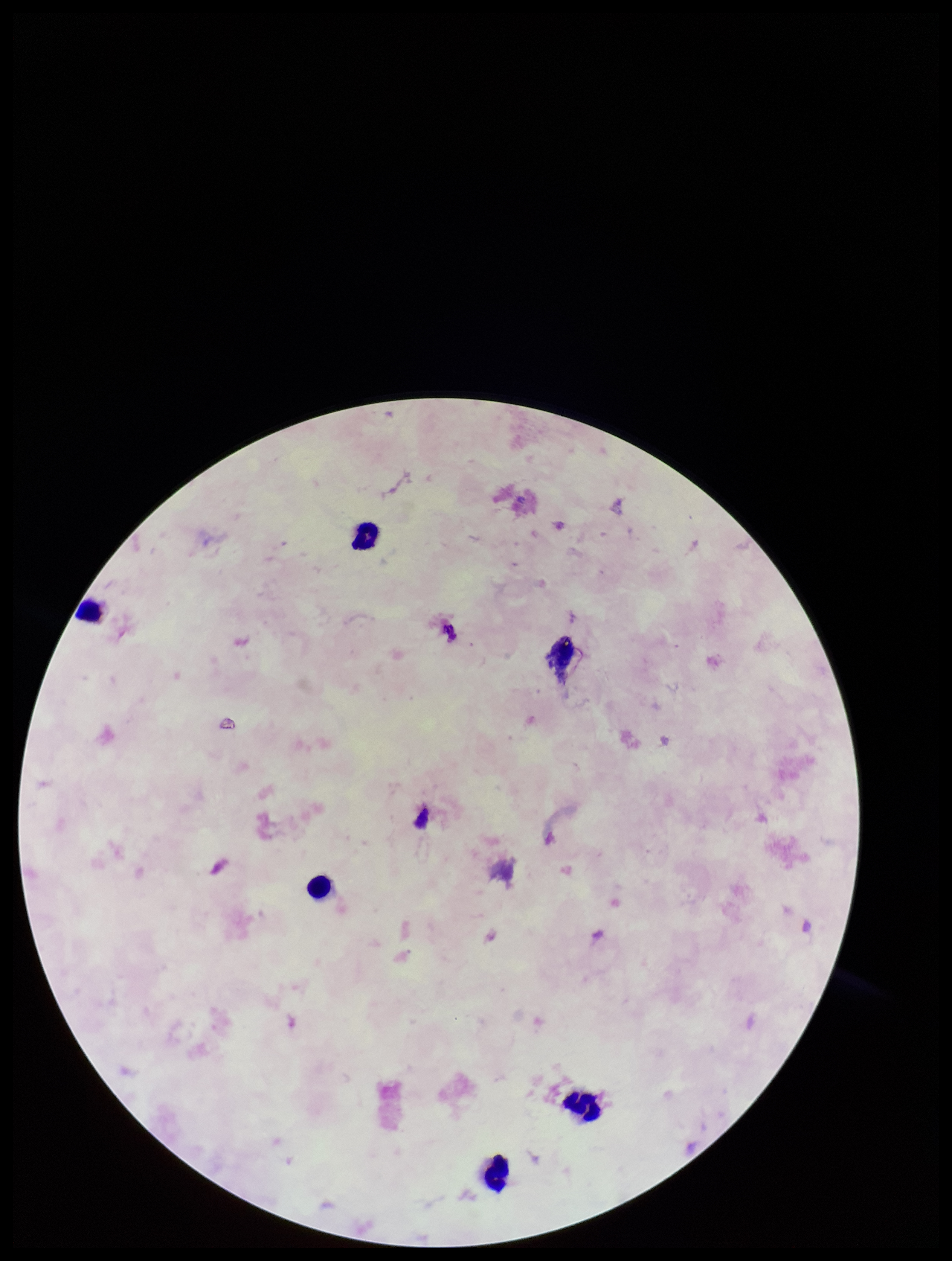

Summary:
  - Field of view: one from this slide
  - Preparation: thick
  - Plasmodium parasites: none detected
  - Stain: Giemsa
  - Leukocyte count: 6
  - Capture: smartphone photograph through the microscope eyepiece
  - Image size: 952×1261 pixels
  - Parasite count: 0
  - Patient malaria status: negative